Name the parasite shown.
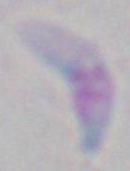

This is Toxoplasma gondii.

Summary:
  - Modality: photomicrograph
  - Magnification: 1000x